Assess this cell for malaria.
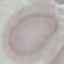
It is uninfected.

Thin smear of blood. Acquired by smartphone through the microscope eyepiece. Cell patch, automatically extracted from a larger field of view and resized to 64 × 64 pixels. Giemsa stain.